Locate every blood parasite and identify its species.
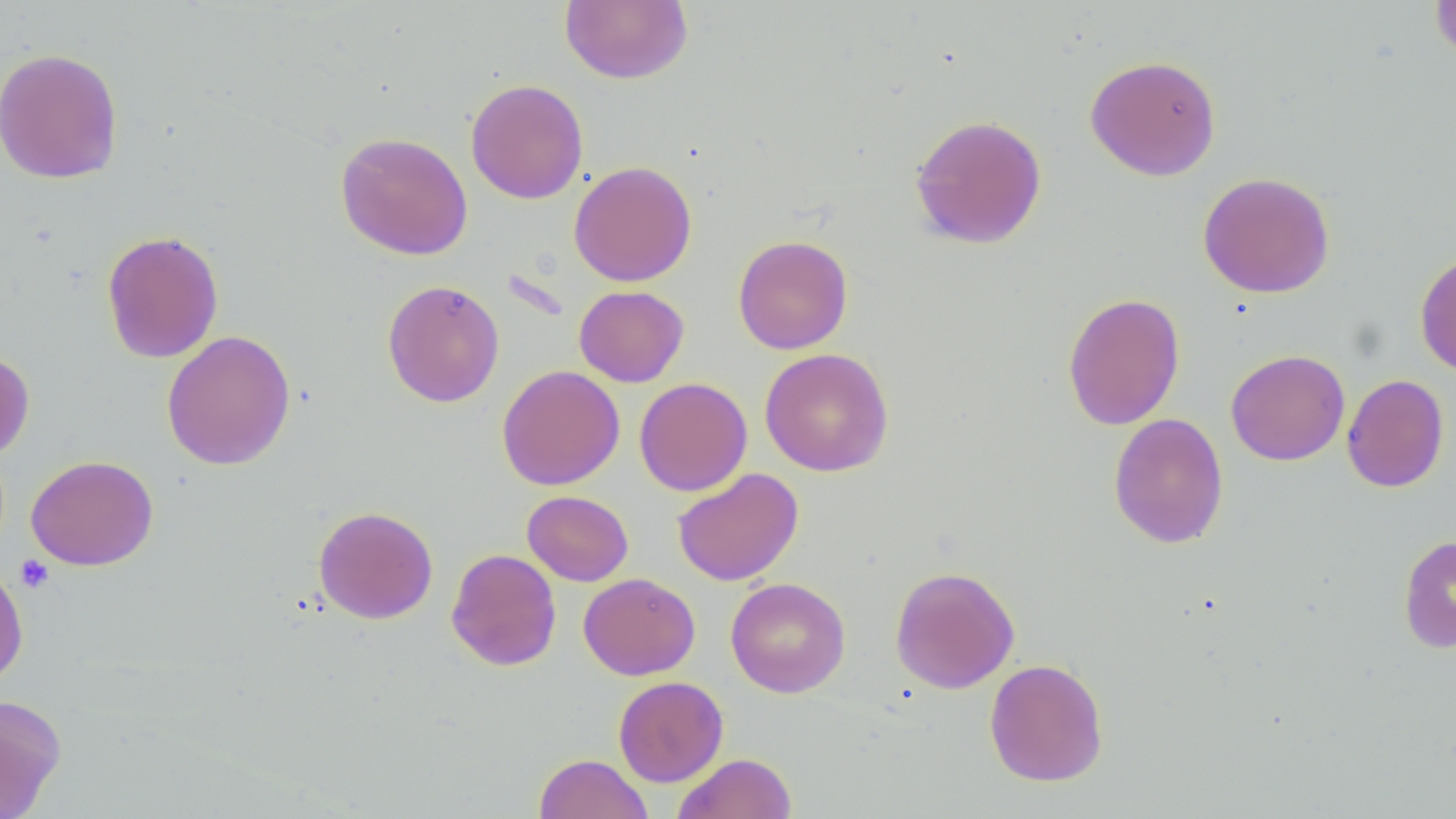

No blood parasites observed.

Approximate bounding boxes as (x1,y1)-(x2,y2) corner pairs in pixels. Uninfected red blood cell locations: (559,0)-(693,84), (1429,0)-(1456,64), (0,47)-(124,184), (1084,54)-(1222,181), (465,78)-(589,204), (909,114)-(1048,250), (335,131)-(473,260), (569,160)-(697,287), (1197,171)-(1335,298), (101,230)-(224,363), (733,234)-(853,354), (1415,250)-(1456,378), (382,279)-(505,408), (574,285)-(689,387), (1062,292)-(1185,430), (161,329)-(296,471), (0,347)-(35,463), (760,347)-(894,477), (1225,349)-(1350,466), (497,365)-(625,490), (1342,374)-(1449,493), (634,377)-(752,496), (1108,413)-(1229,549), (25,454)-(158,571), (672,467)-(803,587), (522,490)-(634,586), (313,505)-(438,624), (1398,535)-(1456,654), (445,548)-(562,671), (0,558)-(28,689), (890,565)-(1019,694), (579,572)-(700,680), (725,577)-(851,698), (984,658)-(1109,787), (613,676)-(728,786), (0,694)-(67,817), (534,753)-(653,819), (673,753)-(797,818). Platelet locations: (14,555)-(55,594). Slide-level diagnosis: no evidence of blood parasites. May-Grünwald-Giemsa stain. Image is 1456×819 pixels. Single field of view. 1000x magnification. Thin blood film. Light microscopy.